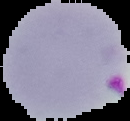

Summary:
  - Image size: 130×121 pixels
  - Image type: cell region segmented out of the field of view; surrounding area masked to black
  - Malaria status: parasitized
  - Preparation: thin blood film